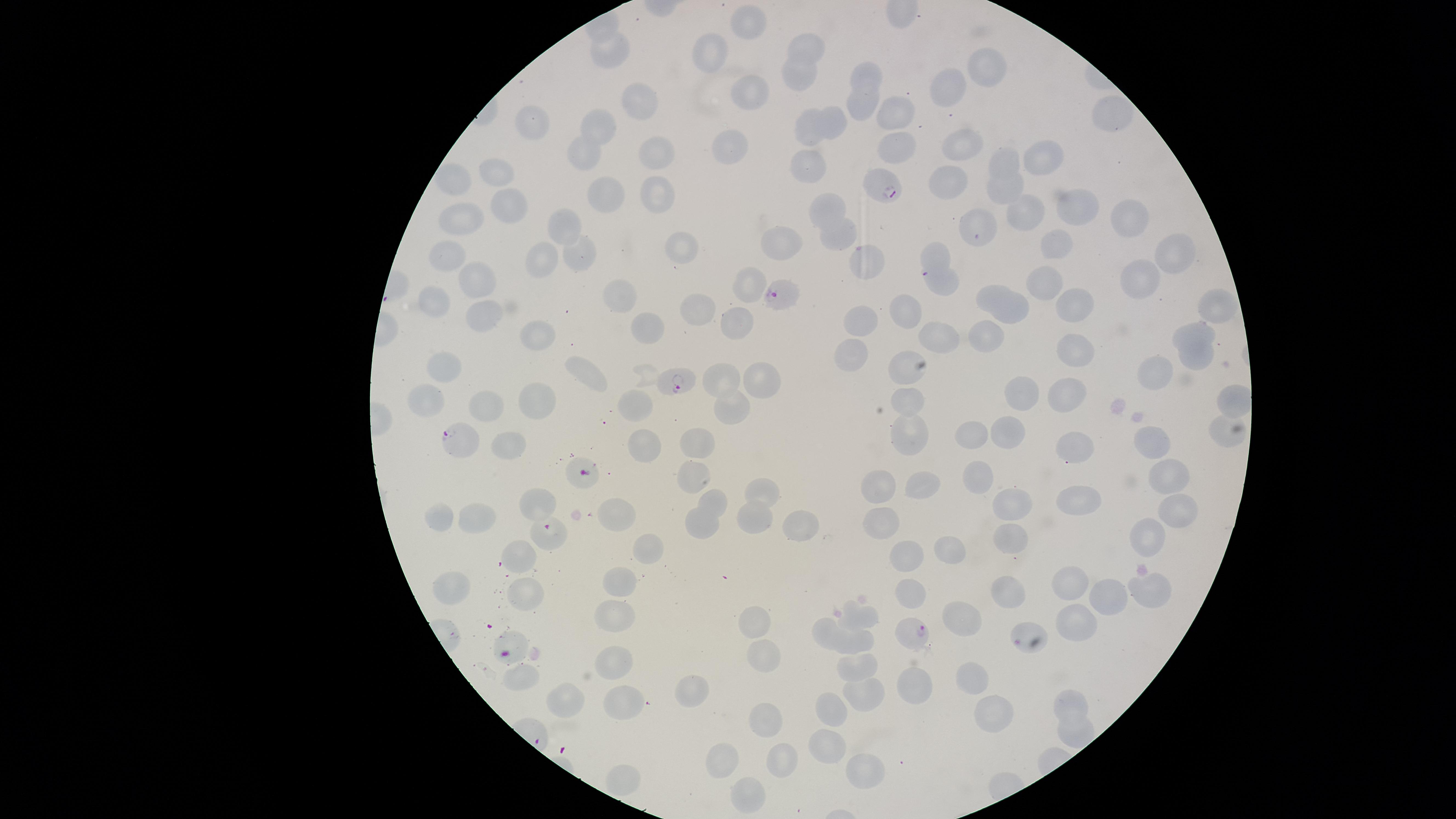 Approximate marker points as {x, y} in pixels. Uninfected red blood cells: {753, 27}, {814, 44}, {609, 49}, {718, 52}, {869, 72}, {992, 72}, {797, 78}, {955, 92}, {751, 93}, {637, 102}, {860, 108}, {1111, 115}, {894, 116}, {535, 122}, {602, 122}, {834, 124}, {804, 128}, {962, 142}, {728, 148}, {895, 153}, {1032, 153}, {658, 155}, {580, 159}, {1003, 161}, {807, 167}, {502, 168}, {452, 180}, {953, 183}, {1003, 189}, {603, 190}, {655, 196}, {510, 206}, {1065, 207}, {826, 208}, {1025, 212}, {1121, 212}, {461, 220}, {979, 222}, {565, 224}, {836, 234}, {783, 238}, {687, 245}, {1061, 245}, {451, 251}, {937, 255}, {545, 256}, {1176, 256}, {580, 260}, {866, 265}, {1141, 277}, {482, 279}, {752, 279}, {945, 284}, {1042, 284}, {988, 293}, {617, 295}, {435, 296}, {1072, 305}, {1219, 305}, {1011, 308}, {906, 312}, {698, 315}, {480, 317}, {861, 320}, {739, 321}, {646, 325}, {988, 331}, {537, 332}, {1198, 333}, {941, 340}, {1075, 352}, {850, 353}, {1196, 358}, {442, 366}, {901, 372}, {584, 375}, {1158, 376}, {720, 377}, {763, 378}, {1025, 388}, {1067, 395}, {429, 397}, {907, 397}, {490, 400}, {632, 402}, {1232, 403}, {733, 404}, {536, 407}, {1005, 429}, {1221, 430}, {908, 431}, {978, 435}, {642, 438}, {1154, 442}, {509, 443}, {697, 443}, {1079, 448}, {1170, 473}, {691, 475}, {874, 482}, {977, 482}, {921, 486}, {764, 491}, {543, 500}, {715, 501}, {1014, 502}, {1076, 503}, {619, 511}, {1179, 514}, {440, 516}, {482, 520}, {750, 523}, {878, 523}, {699, 524}, {800, 528}, {1150, 534}, {1004, 535}, {951, 550}, {640, 552}, {523, 558}, {913, 562}, {616, 581}, {449, 582}, {1076, 582}, {1152, 587}, {1006, 593}, {524, 594}, {906, 597}, {1108, 598}, {959, 612}, {617, 615}, {754, 615}, {867, 615}, {1084, 622}, {825, 628}, {513, 640}, {860, 640}, {765, 659}, {614, 666}, {861, 667}, {967, 673}, {522, 678}, {911, 685}, {694, 692}, {864, 694}, {629, 699}, {570, 701}, {1075, 705}, {995, 707}, {831, 712}, {768, 719}, {1069, 729}, {830, 749}, {726, 761}, {785, 763}, {863, 767}, {623, 784}, {750, 797}. Parasitized red blood cells: {881, 188}, {784, 296}, {675, 382}, {460, 440}, {580, 478}, {545, 533}, {912, 635}. The visible region is circular. Presence: malaria parasites detected. Species: Plasmodium falciparum. Photographed with a smartphone camera through the microscope eyepiece. Giemsa-stained preparation. One field of view of the specimen. Thin smear of blood. Image is 1456×819 pixels.